State the preparation type.
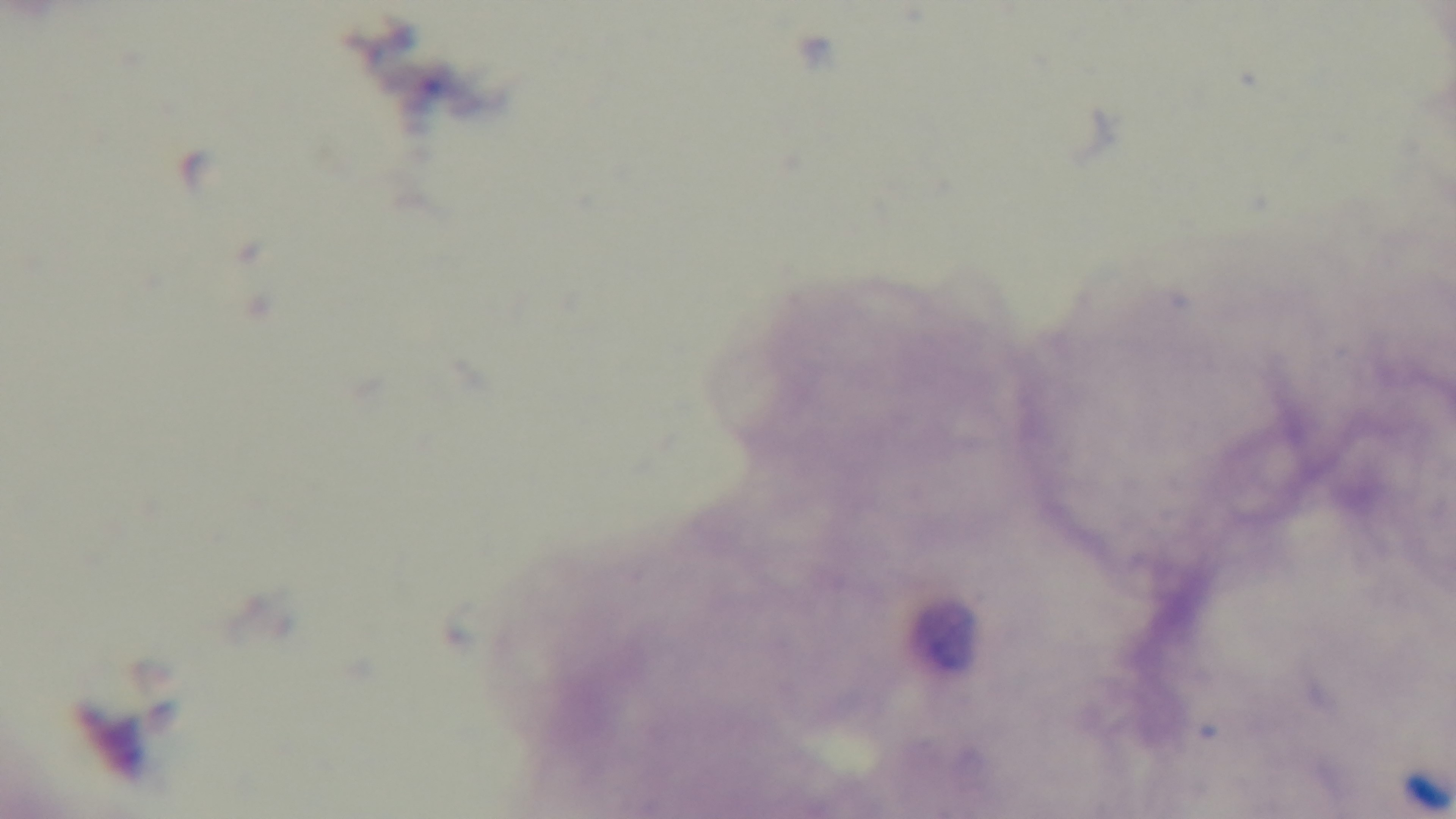

It is a thick blood film.

Photomicrograph. 100x oil-immersion objective. Mounted 4K digital camera. Giemsa-stained. Malaria status: negative. One field from the slide.